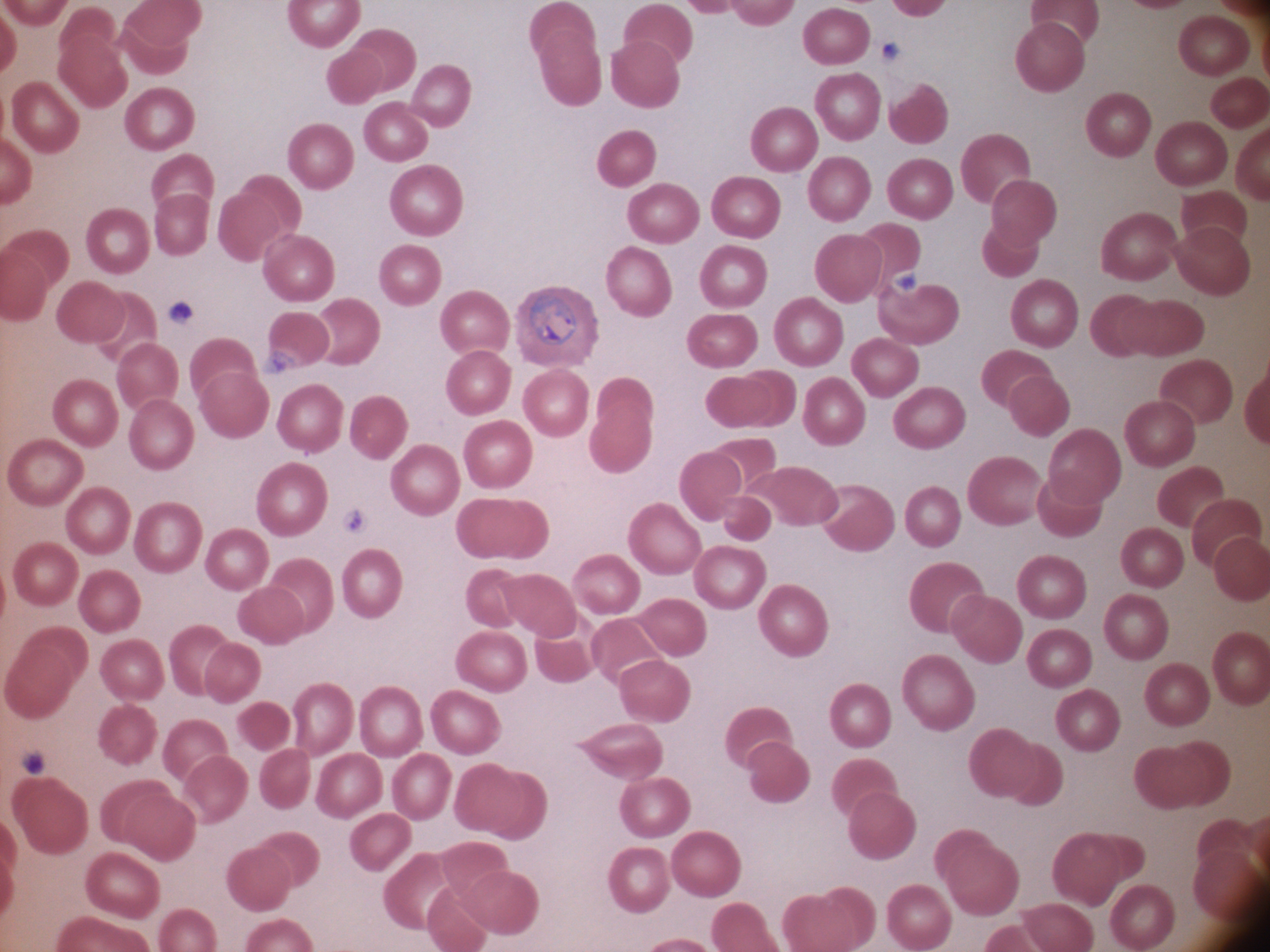

stain: Giemsa
microscope: Leica DM2000 with built-in camera
image_size: 1270×952 pixels
ring_form_locations: 'approximate bounding boxes as [x1, y1, x2, y2] in pixels, from the source annotation, which is not necessarily exhaustive: [529, 294, 577, 346]'
species: Plasmodium ovale
magnification: 100x
preparation: thin blood smear
field_of_view: one from this slide